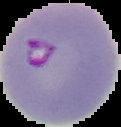 From a thin blood smear. Malaria status: parasitized. Image is 121×127 pixels. Segmented cell region on a black background.